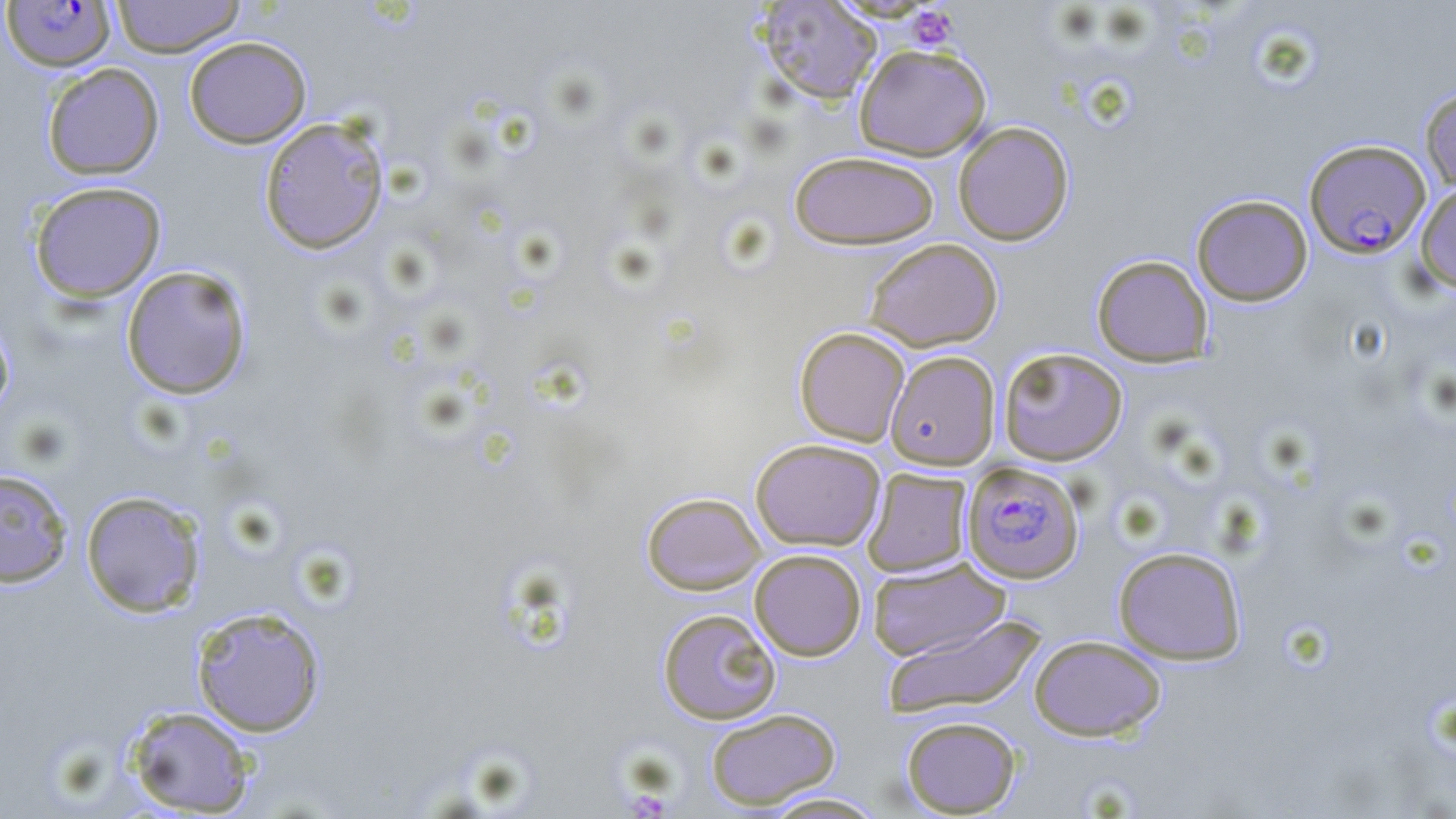

Summary:
  - Coordinate format: approximate bounding boxes as named x1/y1/x2/y2 corners in pixels
  - Plasmodium falciparum-infected red blood cell locations: (x1=1, y1=1, x2=117, y2=73), (x1=1305, y1=138, x2=1431, y2=257), (x1=962, y1=461, x2=1085, y2=583)
  - Platelet locations: (x1=907, y1=5, x2=960, y2=51)
  - Uninfected red blood cell locations: (x1=111, y1=0, x2=246, y2=58), (x1=756, y1=1, x2=882, y2=104), (x1=183, y1=36, x2=312, y2=149), (x1=854, y1=44, x2=992, y2=161), (x1=42, y1=62, x2=164, y2=180), (x1=1419, y1=86, x2=1456, y2=193), (x1=259, y1=116, x2=390, y2=254), (x1=952, y1=121, x2=1074, y2=246), (x1=788, y1=150, x2=940, y2=249), (x1=29, y1=181, x2=167, y2=302), (x1=1415, y1=181, x2=1456, y2=292), (x1=1191, y1=194, x2=1313, y2=306), (x1=863, y1=238, x2=1003, y2=352), (x1=1091, y1=254, x2=1213, y2=367), (x1=121, y1=265, x2=253, y2=400), (x1=0, y1=311, x2=15, y2=422), (x1=794, y1=326, x2=910, y2=446), (x1=998, y1=347, x2=1127, y2=466), (x1=885, y1=350, x2=1000, y2=470), (x1=750, y1=438, x2=885, y2=551), (x1=0, y1=468, x2=73, y2=587), (x1=862, y1=468, x2=973, y2=577), (x1=80, y1=489, x2=206, y2=617), (x1=641, y1=491, x2=766, y2=595), (x1=1113, y1=546, x2=1247, y2=664), (x1=750, y1=548, x2=866, y2=661), (x1=867, y1=557, x2=1011, y2=661), (x1=190, y1=605, x2=327, y2=737), (x1=657, y1=608, x2=781, y2=724), (x1=881, y1=615, x2=1046, y2=720), (x1=1029, y1=634, x2=1166, y2=741), (x1=124, y1=705, x2=257, y2=816), (x1=705, y1=707, x2=841, y2=810), (x1=900, y1=715, x2=1022, y2=817), (x1=758, y1=791, x2=889, y2=818)
  - Slide-level diagnosis: Plasmodium falciparum
  - Modality: light microscopy
  - Stain: May-Grünwald-Giemsa
  - Field of view: single
  - Preparation: thin blood film
  - Image size: 1456×819 pixels
  - Magnification: 1000x